State which parasite is depicted.
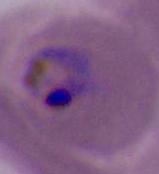

This is Plasmodium.

Captured at either 400x or 1000x magnification. Photomicrograph.